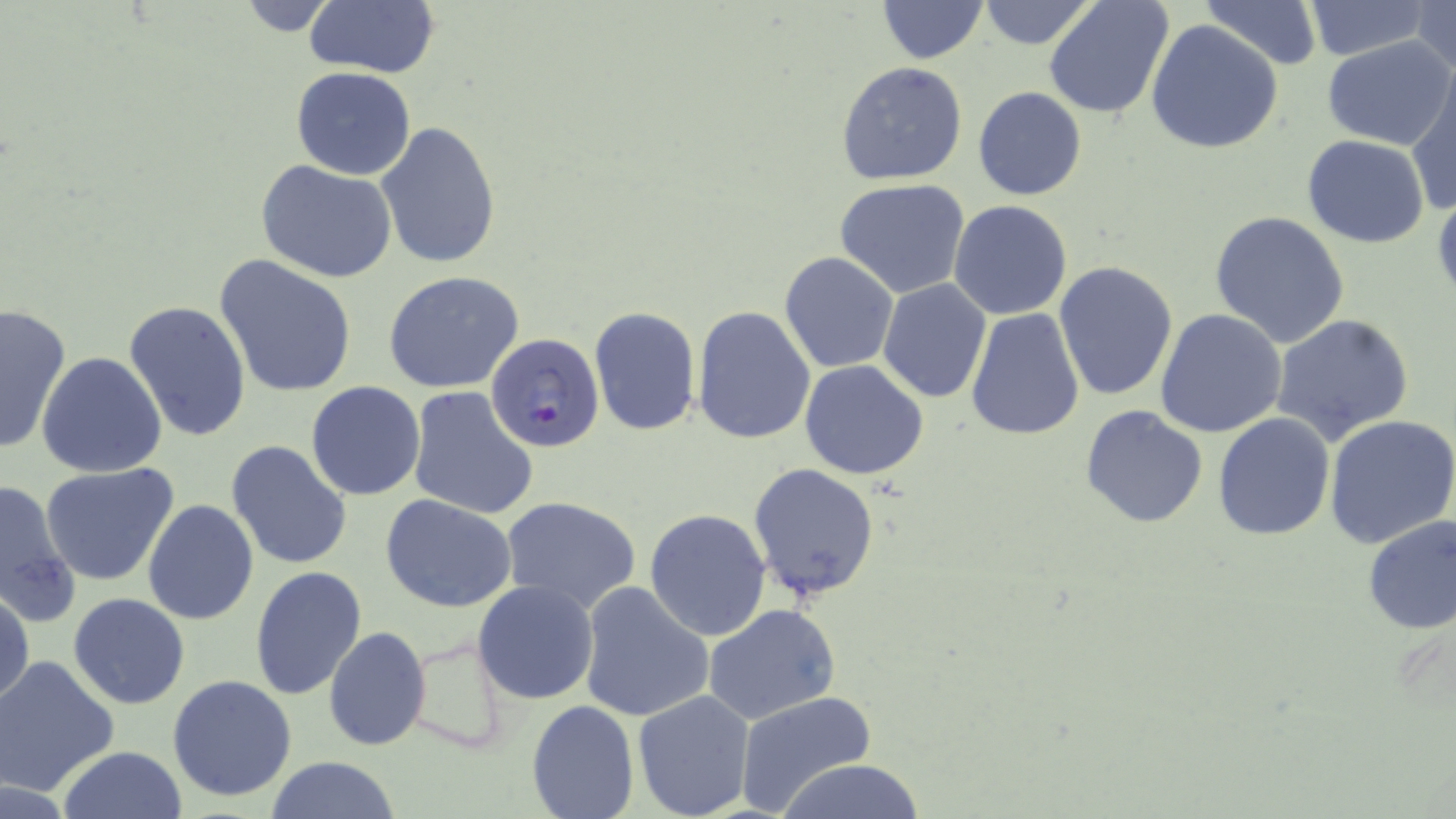
Plasmodium falciparum-infected red blood cell locations = approximate bounding boxes as named x1/y1/x2/y2 corners in pixels: (x1=486, y1=336, x2=608, y2=456)
slide-level diagnosis = Plasmodium falciparum
stain = May-Grünwald-Giemsa
modality = light microscopy
magnification = 1000x
preparation = thin blood smear
uninfected red blood cell locations = approximate bounding boxes as named x1/y1/x2/y2 corners in pixels: (x1=879, y1=0, x2=986, y2=63), (x1=976, y1=0, x2=1096, y2=49), (x1=1045, y1=0, x2=1175, y2=121), (x1=1299, y1=0, x2=1434, y2=60), (x1=1200, y1=1, x2=1323, y2=71), (x1=1409, y1=1, x2=1456, y2=80), (x1=303, y1=2, x2=440, y2=79), (x1=1145, y1=19, x2=1283, y2=155), (x1=1320, y1=36, x2=1456, y2=151), (x1=836, y1=62, x2=968, y2=185), (x1=290, y1=67, x2=416, y2=181), (x1=1406, y1=75, x2=1456, y2=217), (x1=973, y1=86, x2=1087, y2=200), (x1=374, y1=122, x2=504, y2=271), (x1=1301, y1=135, x2=1431, y2=248), (x1=256, y1=159, x2=401, y2=284), (x1=835, y1=178, x2=969, y2=298), (x1=1431, y1=186, x2=1456, y2=306), (x1=949, y1=199, x2=1072, y2=320), (x1=1208, y1=210, x2=1351, y2=348), (x1=779, y1=251, x2=899, y2=373), (x1=215, y1=254, x2=357, y2=399), (x1=1053, y1=261, x2=1179, y2=402), (x1=383, y1=270, x2=526, y2=393), (x1=878, y1=279, x2=992, y2=404), (x1=122, y1=299, x2=252, y2=444), (x1=0, y1=304, x2=74, y2=454), (x1=589, y1=306, x2=701, y2=435), (x1=693, y1=307, x2=817, y2=446), (x1=966, y1=309, x2=1085, y2=442), (x1=1154, y1=309, x2=1287, y2=438), (x1=1270, y1=313, x2=1414, y2=448), (x1=36, y1=352, x2=167, y2=479), (x1=798, y1=360, x2=928, y2=480), (x1=305, y1=381, x2=426, y2=501), (x1=407, y1=386, x2=540, y2=521), (x1=1081, y1=406, x2=1208, y2=528), (x1=1212, y1=412, x2=1336, y2=542), (x1=1325, y1=413, x2=1456, y2=549), (x1=226, y1=440, x2=352, y2=572), (x1=40, y1=462, x2=183, y2=587), (x1=748, y1=462, x2=881, y2=602), (x1=0, y1=475, x2=81, y2=630), (x1=380, y1=493, x2=518, y2=613), (x1=499, y1=495, x2=642, y2=615), (x1=142, y1=499, x2=261, y2=625), (x1=645, y1=508, x2=772, y2=641), (x1=1359, y1=514, x2=1455, y2=635), (x1=250, y1=565, x2=367, y2=700), (x1=472, y1=580, x2=600, y2=703), (x1=577, y1=581, x2=716, y2=723), (x1=0, y1=587, x2=35, y2=712), (x1=68, y1=593, x2=192, y2=710), (x1=703, y1=603, x2=841, y2=726), (x1=323, y1=626, x2=432, y2=752), (x1=401, y1=630, x2=510, y2=752), (x1=1, y1=655, x2=121, y2=796), (x1=168, y1=674, x2=297, y2=802), (x1=632, y1=690, x2=756, y2=819), (x1=733, y1=690, x2=877, y2=817), (x1=526, y1=699, x2=639, y2=819), (x1=56, y1=746, x2=186, y2=819), (x1=264, y1=757, x2=403, y2=818), (x1=771, y1=759, x2=931, y2=818)
image size = 1456×819 pixels
field of view = one of a larger specimen